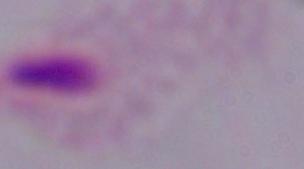

Summary:
  - Modality: micrograph
  - Magnification: 1000x
  - Identification: trichomonad